Find the cells and give the type of each one.
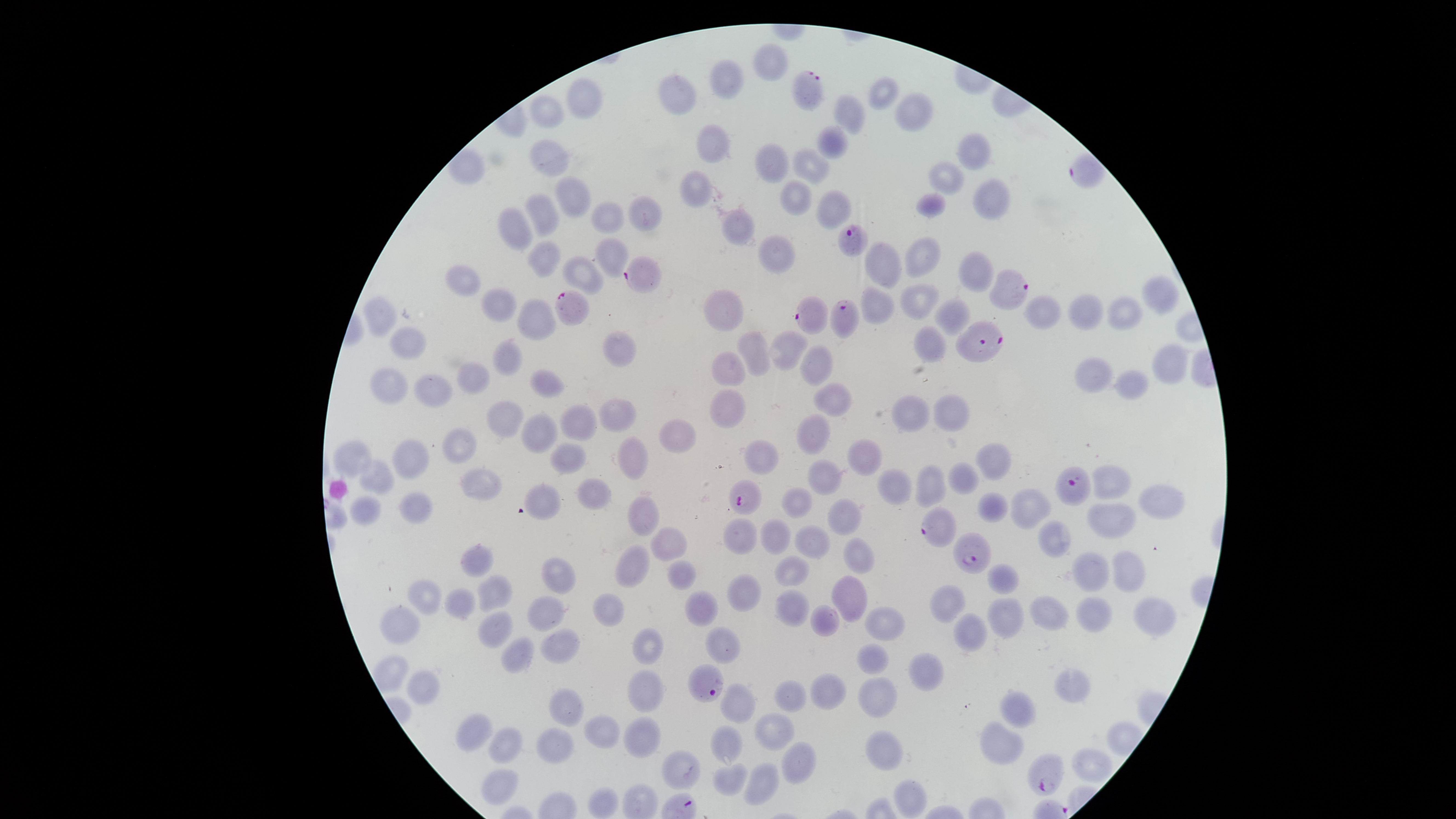

Approximate marker points, in pixels from the top-left corner.
Parasitized RBCs: (x=811, y=93), (x=1083, y=171), (x=856, y=238), (x=642, y=275), (x=1009, y=286), (x=573, y=305), (x=841, y=313), (x=809, y=314), (x=982, y=342), (x=1073, y=487), (x=743, y=503), (x=940, y=530), (x=976, y=552), (x=708, y=686), (x=1047, y=776).
Uninfected RBCs: (x=766, y=62), (x=726, y=80), (x=678, y=92), (x=880, y=92), (x=586, y=100), (x=852, y=110), (x=910, y=110), (x=546, y=112), (x=712, y=141), (x=832, y=142), (x=973, y=148), (x=552, y=156), (x=770, y=162), (x=814, y=164), (x=947, y=178), (x=701, y=184), (x=793, y=193), (x=573, y=194), (x=990, y=202), (x=931, y=206), (x=832, y=208), (x=644, y=209), (x=548, y=210), (x=612, y=216), (x=516, y=225), (x=737, y=229), (x=928, y=249), (x=610, y=251), (x=774, y=251), (x=546, y=257), (x=882, y=258), (x=969, y=271), (x=580, y=279), (x=463, y=284), (x=922, y=300), (x=1156, y=300), (x=877, y=301), (x=502, y=304), (x=727, y=309), (x=1080, y=310), (x=1121, y=311), (x=952, y=313), (x=386, y=314), (x=1044, y=315), (x=540, y=317), (x=931, y=343), (x=408, y=344), (x=788, y=347), (x=622, y=349), (x=754, y=350), (x=509, y=356), (x=816, y=359), (x=1164, y=361), (x=728, y=366), (x=1095, y=372), (x=393, y=378), (x=476, y=378), (x=548, y=382), (x=1133, y=384), (x=435, y=387), (x=827, y=394), (x=950, y=407), (x=725, y=411), (x=614, y=413), (x=913, y=413), (x=505, y=417), (x=572, y=420), (x=814, y=427), (x=541, y=430), (x=672, y=433), (x=459, y=442), (x=867, y=454), (x=569, y=457), (x=768, y=457), (x=357, y=458), (x=626, y=458), (x=418, y=461), (x=993, y=463), (x=826, y=467), (x=377, y=476), (x=966, y=477), (x=477, y=482), (x=896, y=483), (x=592, y=484), (x=934, y=484), (x=1113, y=484), (x=546, y=493), (x=1156, y=495), (x=800, y=499), (x=1032, y=504), (x=420, y=506), (x=992, y=508), (x=643, y=509), (x=366, y=515), (x=841, y=515), (x=1110, y=515), (x=777, y=534), (x=739, y=536), (x=1055, y=537), (x=813, y=540), (x=673, y=545), (x=854, y=556), (x=477, y=557), (x=631, y=564), (x=792, y=567), (x=1090, y=569), (x=1125, y=569), (x=684, y=570), (x=560, y=577), (x=1003, y=580), (x=425, y=594), (x=745, y=594), (x=497, y=598), (x=845, y=600), (x=950, y=603), (x=455, y=605), (x=702, y=609), (x=796, y=611), (x=609, y=612), (x=1051, y=612), (x=1096, y=613), (x=546, y=615), (x=999, y=616), (x=1154, y=616), (x=823, y=620), (x=407, y=621), (x=887, y=623), (x=496, y=630), (x=965, y=632), (x=556, y=641), (x=645, y=642), (x=725, y=644), (x=514, y=650), (x=872, y=656), (x=390, y=668), (x=924, y=671), (x=422, y=685), (x=649, y=685), (x=1069, y=687), (x=831, y=688), (x=792, y=692), (x=878, y=694), (x=1020, y=706), (x=733, y=708), (x=561, y=710), (x=773, y=730), (x=479, y=733), (x=603, y=733), (x=641, y=735), (x=724, y=739), (x=508, y=744), (x=1004, y=744), (x=882, y=746), (x=556, y=749), (x=1096, y=760), (x=678, y=764), (x=793, y=766), (x=731, y=778), (x=764, y=782), (x=499, y=784), (x=910, y=793), (x=598, y=796).
No WBCs identified.

field_of_view: single
species: Plasmodium falciparum
image_size: 1456×819 pixels
visible_region: circular
stain: Giemsa
preparation: thin blood smear
capture: smartphone photograph through the microscope eyepiece